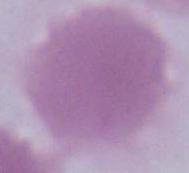

{
  "magnification": "1000x",
  "identification": "erythrocyte",
  "modality": "photomicrograph"
}